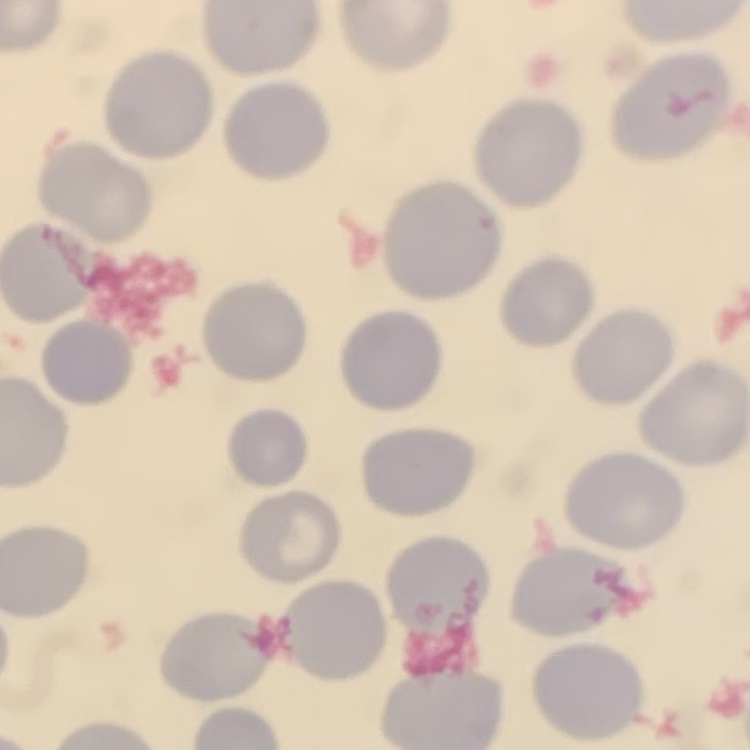
Summary:
  - Erythrocyte morphology: no rouleaux formation
  - Stain: Field's or Giemsa
  - Image type: one tile cut from a larger photomicrograph
  - Preparation: thin blood film